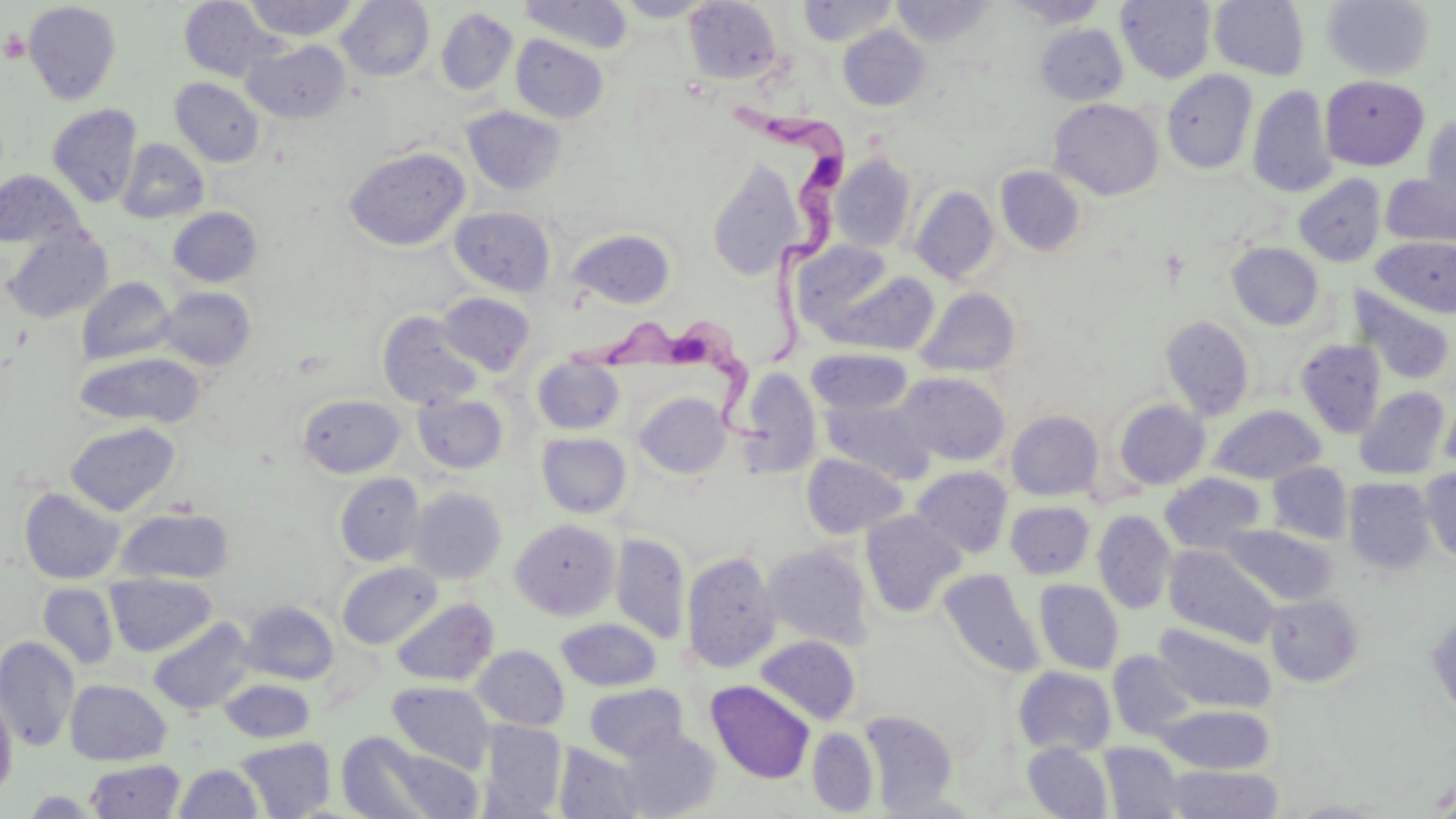
Summary:
  - Coordinate format: approximate bounding boxes as (x1, y1, x2, y2) in pixels
  - Trypanosoma brucei locations: (729, 94, 854, 371), (574, 321, 778, 444)
  - Platelet locations: (2, 31, 30, 62)
  - Uninfected red blood cell locations: (244, 0, 358, 41), (337, 0, 434, 81), (518, 0, 634, 53), (614, 0, 715, 21), (798, 0, 897, 46), (1005, 0, 1109, 28), (1116, 0, 1217, 83), (1209, 0, 1310, 80), (1320, 0, 1435, 81), (23, 1, 122, 105), (179, 1, 277, 81), (683, 1, 783, 85), (891, 1, 997, 46), (1012, 6, 1115, 45), (436, 7, 518, 96), (1035, 23, 1128, 105), (838, 25, 930, 111), (511, 34, 608, 123), (242, 40, 350, 123), (1162, 70, 1258, 175), (1320, 74, 1429, 172), (170, 78, 265, 167), (1248, 86, 1337, 197), (1048, 98, 1164, 201), (47, 104, 143, 207), (462, 105, 567, 196), (1421, 114, 1456, 216), (117, 138, 209, 224), (343, 146, 470, 251), (829, 153, 917, 252), (707, 161, 806, 280), (996, 166, 1085, 256), (0, 170, 86, 248), (1294, 174, 1386, 267), (1380, 174, 1456, 248), (910, 185, 1000, 284), (168, 206, 262, 287), (449, 206, 556, 296), (566, 228, 677, 309), (2, 229, 112, 323), (1371, 236, 1456, 318), (791, 241, 903, 332), (1228, 242, 1324, 330), (812, 267, 940, 357), (77, 277, 175, 365), (158, 286, 256, 370), (1349, 286, 1455, 386), (916, 287, 1020, 378), (437, 292, 535, 375), (378, 311, 483, 410), (1160, 315, 1255, 420), (1295, 338, 1386, 438), (806, 348, 913, 416), (74, 351, 206, 429), (532, 355, 625, 434), (738, 367, 823, 476), (896, 371, 1011, 466), (1354, 386, 1450, 480), (633, 392, 732, 478), (413, 393, 508, 474), (298, 395, 405, 477), (1439, 395, 1456, 477), (821, 397, 934, 484), (1113, 399, 1211, 490), (1209, 405, 1326, 484), (1006, 410, 1104, 501), (65, 421, 181, 515), (537, 432, 632, 518), (802, 453, 907, 539), (1266, 462, 1353, 544), (911, 466, 1013, 558), (1420, 466, 1456, 566), (1160, 472, 1266, 553), (335, 473, 425, 566), (1344, 477, 1436, 574), (408, 487, 506, 584), (20, 488, 125, 584), (1005, 501, 1095, 579), (115, 506, 234, 584), (1093, 510, 1176, 614), (860, 511, 967, 618), (510, 518, 620, 621), (1222, 524, 1337, 605), (610, 533, 690, 644), (762, 542, 874, 649), (1163, 544, 1280, 647), (682, 550, 781, 673), (337, 562, 443, 649), (938, 568, 1044, 678), (106, 573, 217, 656), (1034, 579, 1124, 674), (38, 583, 119, 669), (1265, 594, 1364, 688), (391, 597, 498, 686), (239, 601, 339, 685), (1426, 611, 1456, 724), (148, 617, 255, 715), (557, 618, 662, 692), (1153, 623, 1276, 714), (755, 635, 861, 725), (0, 636, 80, 751), (472, 645, 569, 731), (1109, 650, 1198, 741), (1013, 666, 1116, 756), (219, 677, 315, 744), (64, 679, 172, 765), (707, 680, 815, 784), (387, 681, 495, 773), (583, 684, 688, 762), (0, 690, 18, 798), (1156, 704, 1275, 775), (859, 710, 958, 813), (481, 719, 567, 817), (613, 726, 722, 818), (807, 727, 879, 816), (336, 732, 442, 819), (234, 736, 336, 819), (554, 742, 648, 819), (1099, 742, 1187, 819), (372, 743, 484, 817), (1023, 743, 1113, 819), (85, 759, 186, 818), (174, 764, 263, 818), (1163, 765, 1284, 819), (1283, 800, 1398, 818)
  - Slide-level diagnosis: Trypanosoma brucei
  - Stain: May-Grünwald-Giemsa
  - Field of view: single
  - Magnification: 1000x
  - Modality: optical microscopy
  - Preparation: thin blood smear
  - Image size: 1456×819 pixels